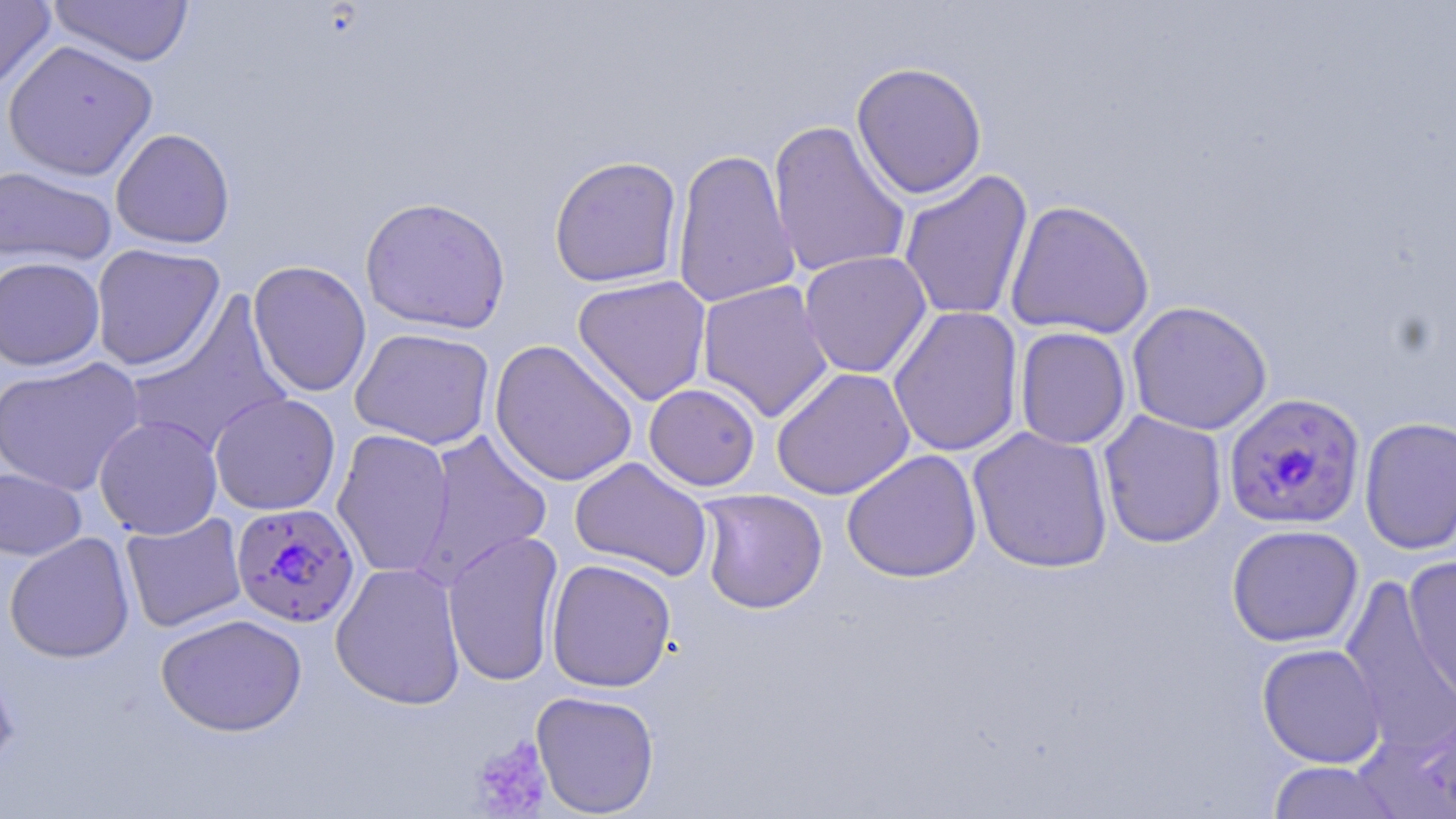
Summary:
  - Coordinate format: approximate bounding boxes as [x1, y1, x2, y2] in pixels
  - Plasmodium falciparum-infected red blood cell locations: [1223, 392, 1366, 530], [229, 502, 358, 627]
  - Uninfected red blood cell locations: [0, 0, 56, 95], [47, 0, 196, 67], [3, 40, 158, 181], [851, 61, 988, 199], [767, 119, 911, 279], [111, 128, 235, 249], [671, 147, 800, 310], [549, 155, 683, 288], [0, 165, 116, 268], [898, 170, 1034, 323], [360, 196, 511, 334], [1004, 199, 1155, 339], [90, 243, 226, 371], [798, 251, 933, 378], [0, 256, 105, 371], [247, 260, 372, 397], [572, 275, 712, 406], [696, 279, 834, 422], [123, 294, 293, 458], [1126, 300, 1272, 435], [887, 305, 1024, 457], [1014, 326, 1132, 450], [350, 327, 496, 450], [489, 339, 639, 488], [0, 357, 145, 497], [771, 367, 915, 500], [643, 383, 761, 491], [209, 392, 341, 516], [1098, 411, 1227, 549], [94, 415, 223, 540], [1359, 416, 1456, 555], [967, 426, 1114, 574], [332, 429, 454, 579], [413, 429, 553, 586], [842, 449, 982, 583], [570, 456, 713, 582], [0, 467, 87, 561], [696, 488, 828, 614], [120, 512, 247, 633], [1226, 523, 1363, 648], [442, 529, 564, 687], [4, 533, 135, 663], [1403, 555, 1456, 710], [546, 558, 677, 692], [330, 561, 467, 710], [1339, 574, 1456, 756], [155, 612, 307, 736], [1257, 643, 1386, 768], [0, 663, 19, 778], [531, 690, 660, 817], [1266, 760, 1403, 818]
  - Platelet locations: [469, 736, 552, 817]
  - Slide-level diagnosis: Plasmodium falciparum
  - Image size: 1456×819 pixels
  - Preparation: thin blood smear
  - Modality: optical microscopy
  - Stain: May-Grünwald-Giemsa
  - Field of view: single
  - Magnification: 1000x